Outline each Plasmodium falciparum-infected red blood cell.
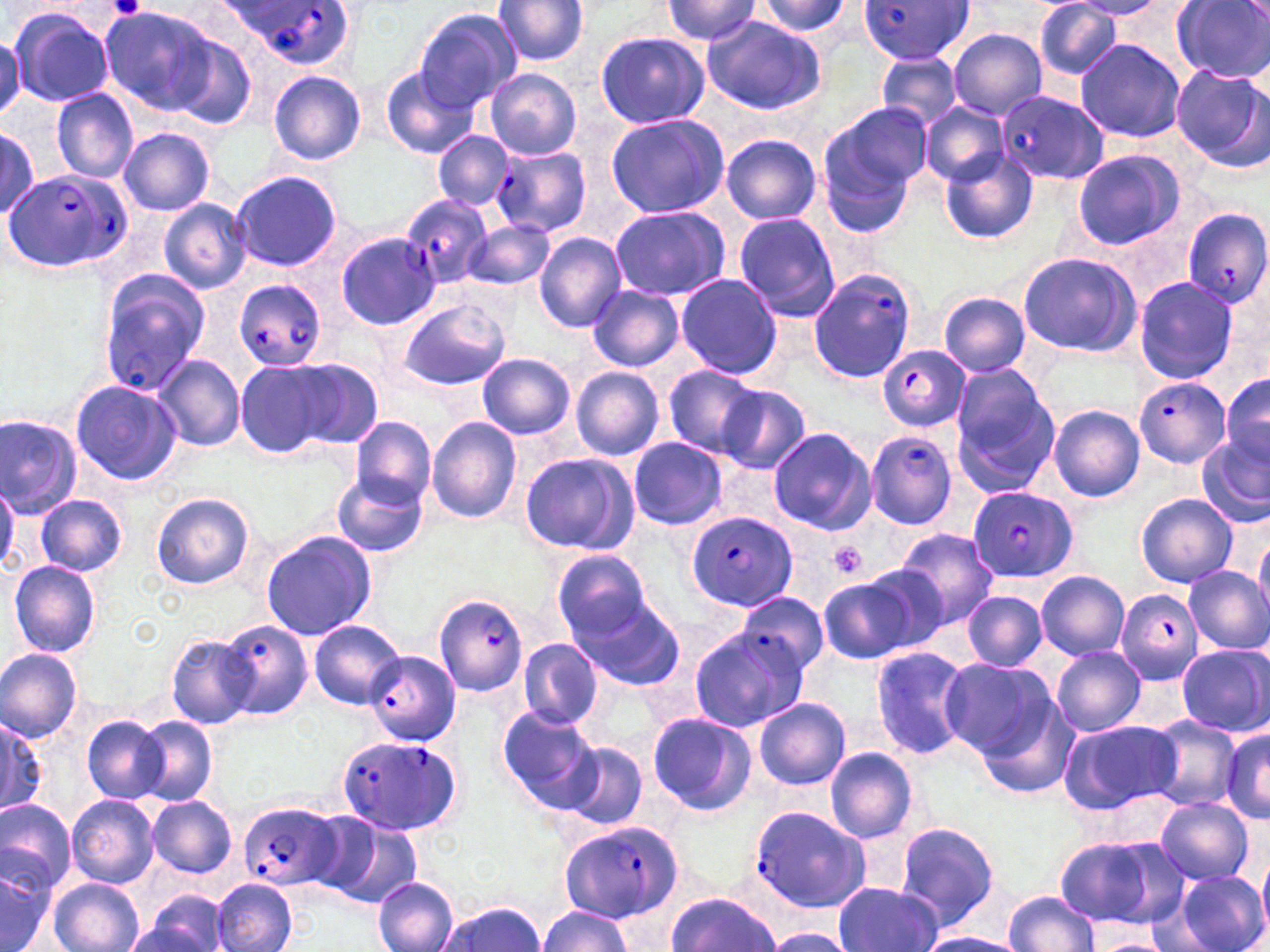
Approximate bounding boxes as (x1, y1, x2, y2) in pixels.
Plasmodium falciparum-infected red blood cells: (223, 0, 357, 65), (856, 0, 974, 64), (996, 90, 1109, 185), (490, 146, 591, 238), (5, 168, 133, 271), (400, 192, 493, 289), (1182, 208, 1270, 310), (337, 232, 440, 330), (807, 267, 917, 385), (96, 274, 208, 397), (234, 280, 327, 372), (875, 345, 971, 432), (1133, 376, 1230, 468), (866, 430, 958, 531), (966, 487, 1078, 583), (687, 510, 797, 612), (1115, 589, 1204, 684), (434, 593, 530, 696), (735, 593, 828, 678), (361, 651, 461, 746), (339, 735, 460, 834), (238, 802, 340, 890), (749, 806, 873, 913), (557, 820, 686, 922).

Summary:
  - Platelet locations: (108, 0, 148, 18), (827, 542, 867, 580)
  - Uninfected red blood cell locations: (491, 0, 590, 66), (753, 0, 853, 37), (657, 1, 765, 47), (1033, 2, 1124, 81), (1172, 2, 1270, 82), (6, 4, 116, 107), (100, 5, 222, 114), (414, 6, 522, 110), (702, 16, 827, 116), (949, 29, 1046, 119), (596, 32, 708, 129), (169, 37, 257, 131), (1074, 38, 1187, 143), (877, 52, 965, 134), (380, 64, 482, 159), (1172, 66, 1270, 174), (485, 69, 581, 160), (269, 70, 366, 166), (50, 89, 141, 184), (815, 103, 930, 234), (920, 103, 1009, 185), (606, 113, 730, 218), (0, 123, 41, 223), (118, 127, 214, 216), (434, 130, 512, 211), (721, 135, 821, 225), (1071, 149, 1185, 251), (938, 152, 1038, 246), (227, 171, 343, 272), (158, 198, 253, 294), (608, 204, 731, 300), (734, 211, 840, 323), (463, 220, 554, 289), (533, 231, 627, 333), (1018, 252, 1142, 357), (675, 272, 784, 380), (1131, 275, 1241, 385), (587, 285, 684, 372), (939, 291, 1032, 378), (398, 300, 511, 390), (155, 353, 246, 452), (477, 354, 575, 438), (289, 358, 383, 447), (235, 360, 330, 457), (950, 366, 1060, 494), (571, 367, 664, 460), (662, 367, 767, 458), (1221, 370, 1270, 475), (71, 379, 182, 485), (716, 384, 812, 475), (1048, 405, 1146, 502), (0, 412, 83, 518), (352, 416, 436, 507), (427, 416, 521, 523), (768, 427, 876, 535), (1196, 435, 1270, 530), (627, 438, 729, 530), (518, 452, 638, 554), (332, 472, 429, 557), (0, 482, 20, 572), (150, 492, 254, 590), (1134, 493, 1237, 588), (36, 495, 126, 576), (893, 529, 999, 630), (261, 530, 378, 640), (1254, 533, 1270, 622), (553, 550, 651, 643), (9, 561, 103, 658), (1183, 566, 1270, 656), (818, 569, 938, 664), (1037, 569, 1130, 659), (962, 591, 1047, 671), (574, 596, 685, 691), (218, 619, 312, 720), (307, 620, 405, 708), (688, 629, 803, 733), (165, 634, 258, 729), (517, 639, 602, 730), (870, 645, 972, 761), (1177, 645, 1270, 735), (1051, 646, 1146, 736), (0, 648, 83, 743), (938, 658, 1054, 758), (977, 692, 1079, 797), (754, 697, 852, 790), (497, 706, 603, 811), (646, 712, 757, 816), (0, 714, 47, 819), (81, 715, 167, 802), (1145, 716, 1241, 811), (135, 717, 218, 805), (1059, 719, 1182, 815), (1219, 726, 1270, 826), (560, 741, 647, 830), (824, 747, 919, 843), (147, 794, 238, 878), (67, 795, 158, 888), (1156, 797, 1254, 884), (0, 800, 77, 896), (321, 816, 422, 907), (894, 822, 1000, 931), (1054, 833, 1189, 930), (1259, 857, 1270, 935), (0, 859, 52, 952), (1176, 871, 1267, 952), (48, 877, 143, 952), (373, 877, 459, 952), (211, 878, 296, 952), (835, 881, 941, 952), (132, 890, 234, 952), (1003, 890, 1099, 951), (664, 892, 778, 950), (437, 901, 547, 952), (537, 905, 633, 952), (918, 933, 1027, 952), (1091, 937, 1172, 952)
  - Slide-level diagnosis: Plasmodium falciparum
  - Modality: optical microscopy
  - Image size: 1270×952 pixels
  - Stain: May-Grünwald-Giemsa
  - Preparation: thin blood smear
  - Magnification: 1000x
  - Field of view: single